State the preparation type.
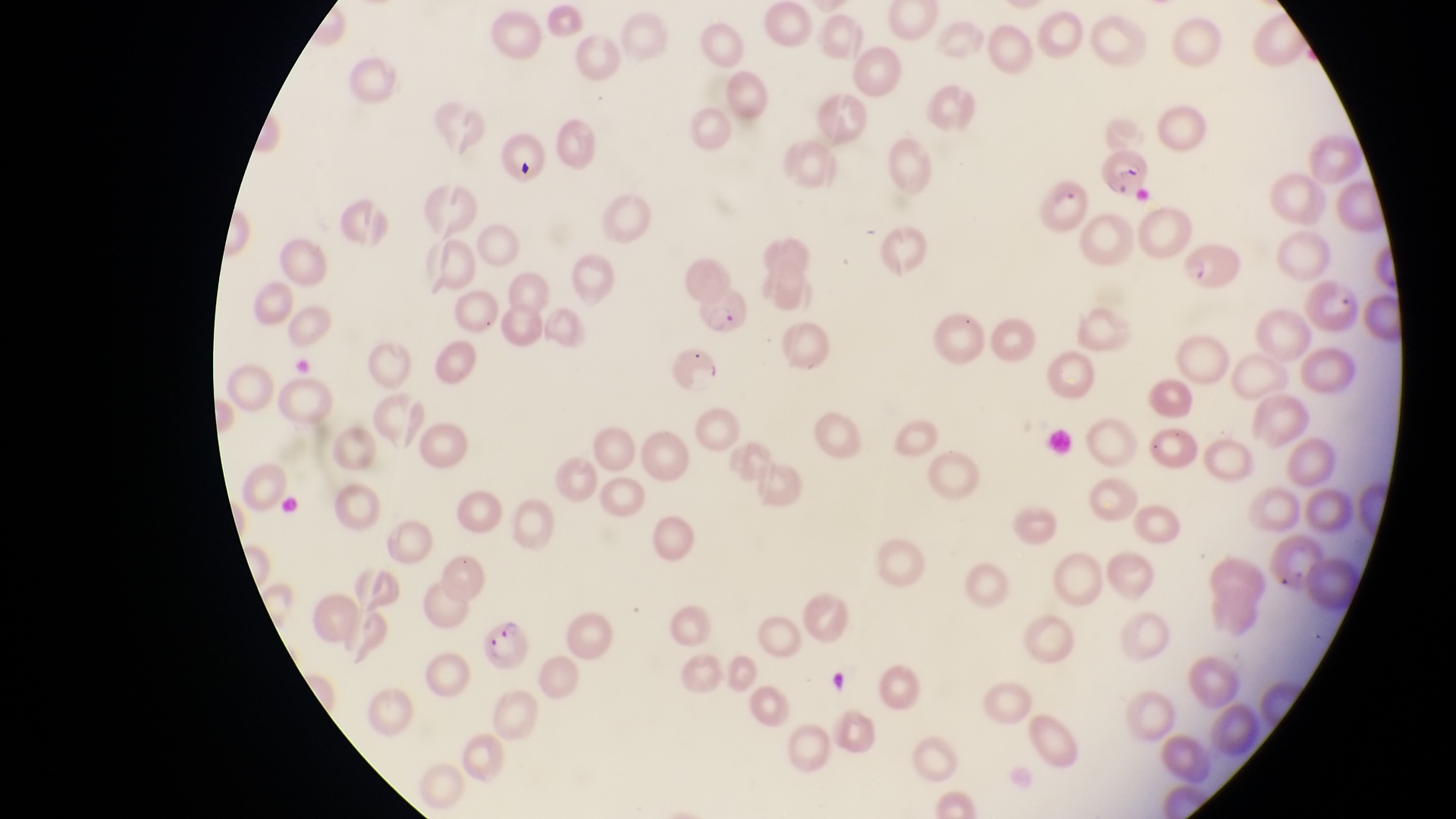

Thin blood film.

Approximate bounding boxes as {left, top, right, bottom} in pixels. Artifact (platelet-like body, stain precipitate, or debris) locations: {508, 153, 545, 185}. Parasitised red blood cell locations: {1107, 146, 1154, 198}, {1036, 180, 1088, 236}, {1178, 244, 1245, 294}, {1305, 274, 1364, 335}, {698, 281, 748, 336}, {671, 346, 723, 393}, {481, 614, 531, 664}. Image is 1456×819 pixels. Photographed through the eyepiece of an Olympus CX-23 microscope with a smartphone camera. Sample from Uganda. Single field of view. Magnification of 1000x.